Point out each Plasmodium parasite.
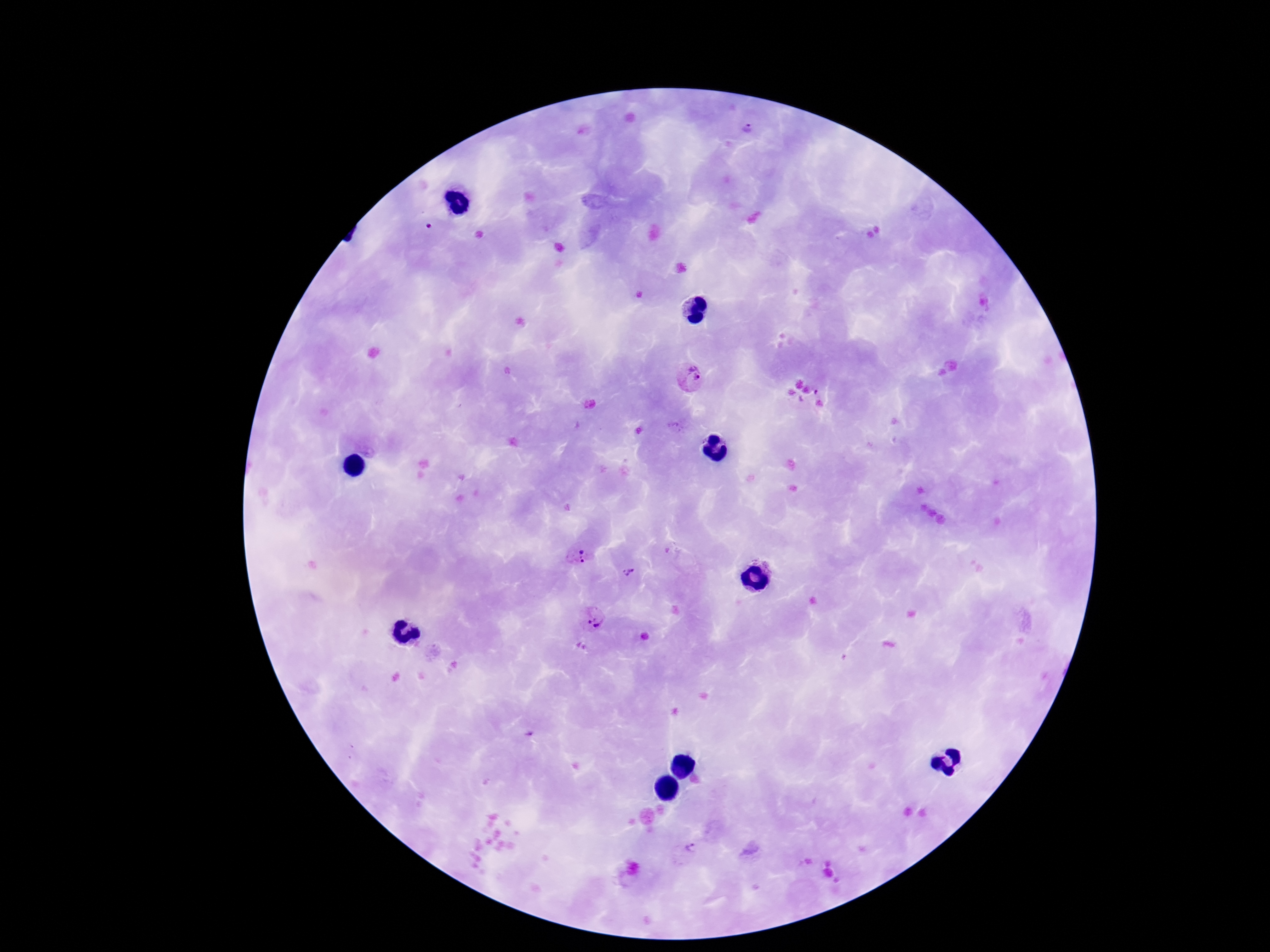
Approximate centers as [x, y] in pixels.
Plasmodium parasites: [749, 130], [691, 378], [578, 557], [633, 573], [592, 620], [643, 637], [687, 853].

capture = smartphone camera through the microscope eyepiece
field of view = single
stain = Giemsa
magnification = 100x
preparation = thick blood film
patient malaria status = positive
image size = 1270×952 pixels